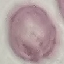

Summary:
  - Malaria status: uninfected
  - Stain: Giemsa
  - Image type: automatically extracted cell patch, resized to 64 × 64 pixels
  - Preparation: thin smear
  - Capture: smartphone through the microscope eyepiece